Locate every Plasmodium parasite.
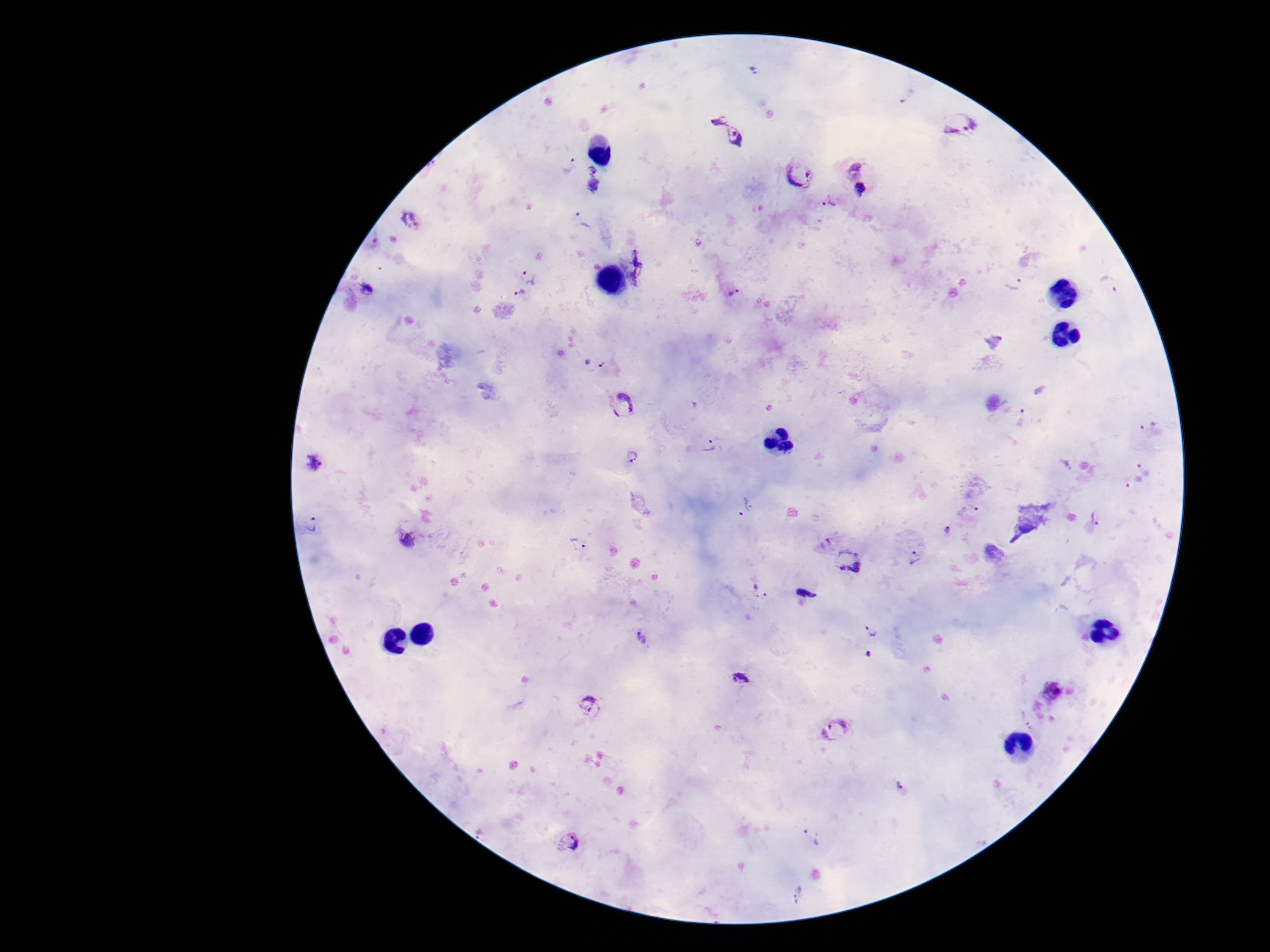

Approximate centers as [x, y] in pixels.
Plasmodium parasites: [753, 70], [904, 94], [717, 119], [959, 127], [735, 136], [565, 162], [855, 165], [801, 175], [593, 180], [861, 193], [829, 202], [410, 221], [582, 221], [640, 265], [533, 275], [1014, 283], [1110, 286], [372, 292], [732, 294], [517, 298], [596, 363], [623, 404], [1023, 418], [1150, 429], [712, 445], [631, 458], [312, 463], [1069, 465], [1145, 467], [1134, 484], [746, 509], [968, 510], [1096, 518], [313, 525], [948, 532], [410, 541], [575, 542], [823, 542], [914, 558], [847, 563], [759, 593], [805, 595], [872, 632], [643, 639], [867, 654], [741, 680], [1055, 690], [589, 705], [835, 729], [901, 785], [811, 836], [568, 840], [799, 893].

Patient malaria status: infected. Image is 1270×952 pixels. Giemsa stain. 100x magnification. Photographed through the microscope eyepiece with a smartphone camera. Thick blood film. One field from this slide.